Locate every Plasmodium parasite.
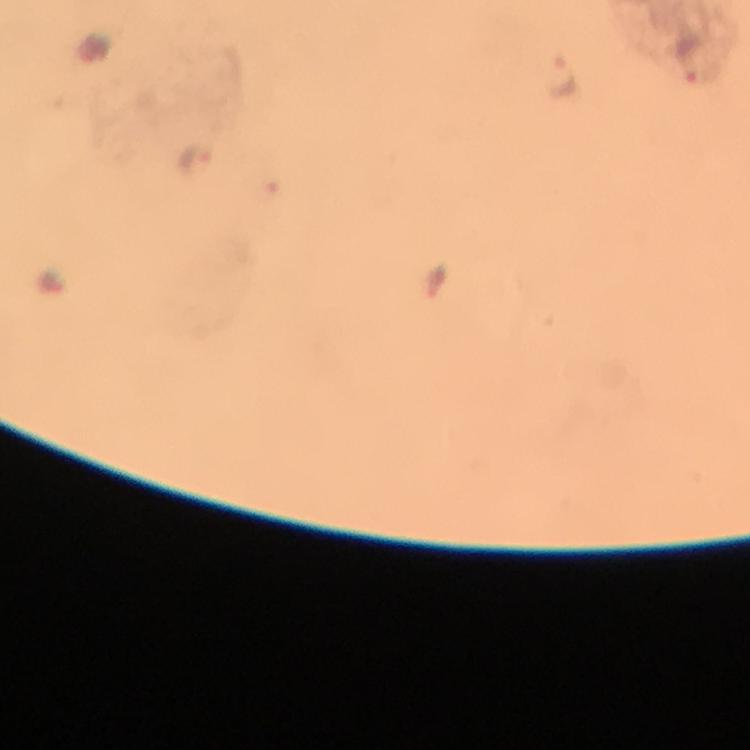
Approximate centers as {x, y} in pixels.
Plasmodium parasites: {690, 59}, {561, 78}, {199, 161}.

Summary:
  - Capture: smartphone photograph through a microscope
  - Magnification: 100x
  - Immersion oil: used
  - Preparation: thick smear
  - Cropped from: a single field of view
  - Stain: Giemsa
  - Context: from a diagnostic examination for malaria
  - Image size: 750×750 pixels